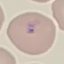

Summary:
  - Result: malaria parasites detected
  - Stain: Giemsa
  - Capture: smartphone through the microscope eyepiece
  - Preparation: thin smear
  - Image type: cell patch, automatically extracted from a larger field of view and resized to 64 × 64 pixels